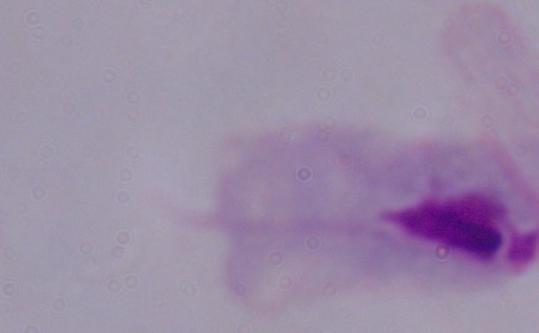

Summary:
  - Magnification: 1000x
  - Identification: trichomonad
  - Modality: micrograph